Find each white blood cell.
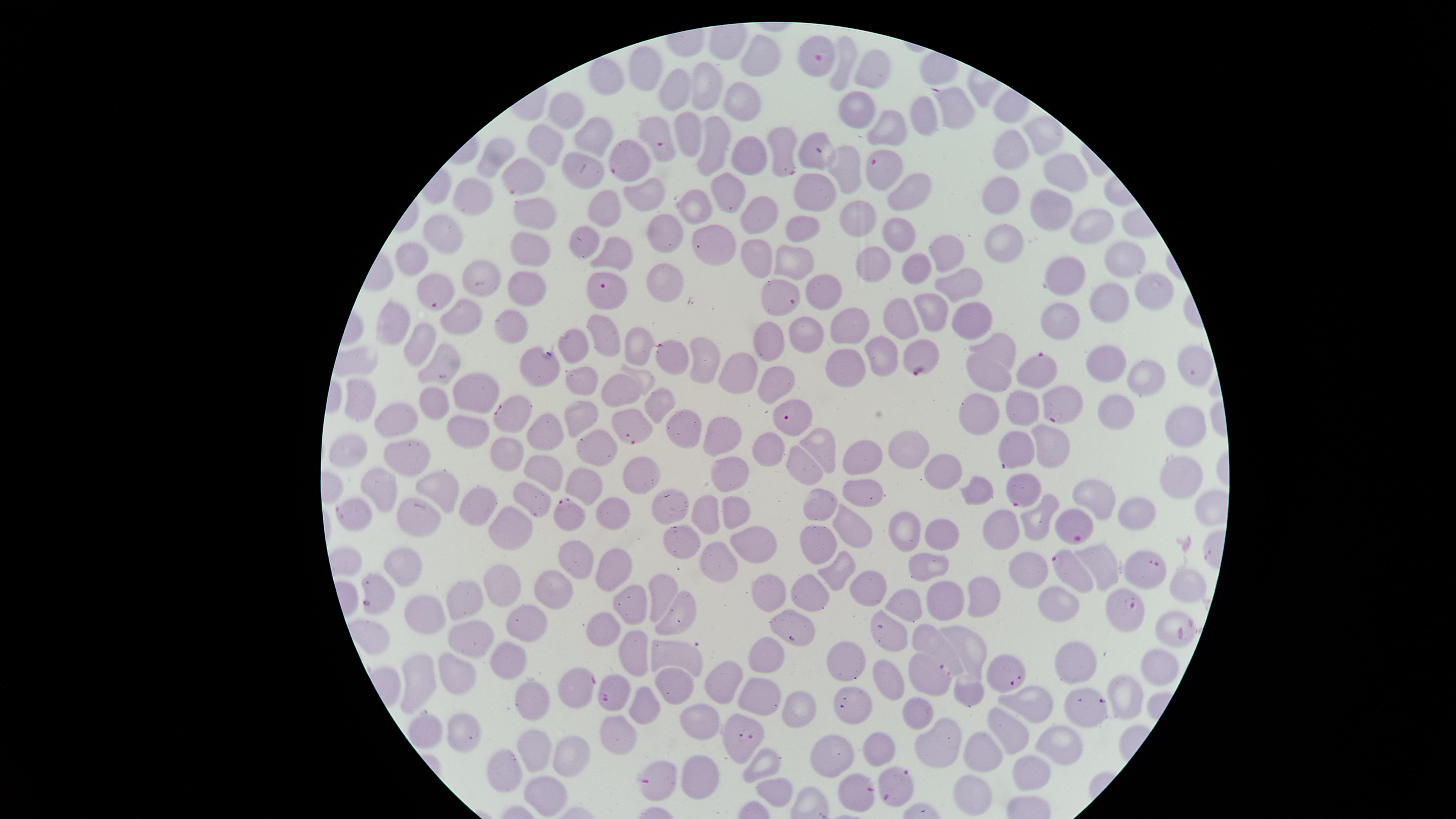

No white blood cells identified.

field of view = single
image size = 1456×819 pixels
parasitized red blood cells = approximate marker points as (x, y) in pixels: (819, 57), (949, 103), (658, 134), (780, 146), (815, 152), (627, 161), (884, 164), (521, 175), (609, 289), (439, 293), (781, 296), (671, 357), (919, 358), (1038, 370), (1062, 402), (514, 415), (793, 416), (629, 424), (1013, 448), (1021, 492), (361, 512), (568, 514), (1074, 525), (1070, 571), (1152, 573), (1126, 605), (1001, 670), (925, 672), (581, 685), (610, 695), (743, 738), (658, 777), (896, 786), (856, 795)
preparation = thin blood smear
species = Plasmodium falciparum
presence = malaria parasites seen
uninfected red blood cells = approximate marker points as (x, y) in pixels: (759, 57), (846, 68), (649, 72), (873, 72), (606, 75), (712, 86), (680, 88), (748, 99), (569, 109), (857, 111), (921, 115), (890, 129), (1045, 133), (686, 134), (596, 137), (714, 142), (548, 146), (1011, 150), (499, 154), (745, 154), (582, 161), (850, 166), (1070, 171), (911, 185), (642, 186), (815, 188), (729, 194), (1003, 194), (475, 195), (605, 202), (1050, 206), (696, 209), (859, 213), (536, 214), (756, 215), (1097, 218), (799, 228), (586, 234), (664, 234), (900, 236), (1012, 239), (440, 245), (947, 245), (713, 248), (527, 252), (616, 252), (418, 254), (1128, 258), (870, 260), (753, 263), (793, 267), (921, 267), (1067, 270), (485, 278), (964, 279), (668, 281), (526, 287), (819, 289), (1151, 293), (1111, 300), (931, 309), (903, 311), (459, 313), (396, 320), (1058, 320), (511, 322), (972, 323), (850, 326), (807, 332), (607, 334), (422, 339), (764, 340), (577, 342), (882, 348), (637, 349), (1007, 351), (1104, 356), (703, 361), (440, 363), (1197, 363), (844, 368), (739, 370), (539, 372), (985, 376), (583, 377), (645, 378), (775, 380), (1145, 380), (613, 387), (473, 389), (362, 396), (438, 404), (660, 404), (1028, 406), (972, 410), (1118, 410), (396, 417), (579, 418), (541, 427), (1186, 428), (470, 429), (685, 430), (719, 435), (1058, 445), (816, 447), (595, 448), (763, 449), (503, 451), (914, 451), (343, 455), (405, 456), (862, 457), (806, 463), (545, 471), (637, 473), (943, 473), (729, 475), (1179, 475), (379, 485), (583, 485), (978, 487), (441, 489), (861, 493), (1094, 493), (816, 500), (530, 503), (484, 505), (670, 509), (733, 510), (1138, 510), (616, 511), (705, 513), (420, 517), (854, 525), (1005, 525), (1036, 526), (509, 527), (906, 532), (941, 535), (679, 541), (748, 544), (813, 549), (578, 561), (712, 562), (614, 563), (394, 564), (927, 565), (1105, 567), (833, 569), (1033, 576), (501, 584), (1178, 586), (866, 587), (765, 592), (552, 593), (984, 595), (662, 596), (809, 598), (1062, 601), (951, 602), (466, 604), (908, 604), (636, 606), (431, 613), (679, 616), (529, 617), (799, 625), (1171, 626), (610, 627), (469, 633), (894, 635), (931, 641), (964, 648), (635, 649), (679, 650), (514, 655), (1158, 658), (769, 662), (1071, 662), (852, 665), (451, 674), (882, 679), (421, 682), (723, 682), (675, 683), (1120, 693), (968, 695), (532, 696), (757, 699), (1081, 699), (1034, 701), (849, 702), (647, 704), (795, 709), (917, 711), (694, 715), (1010, 729), (458, 731), (426, 732), (619, 732), (946, 742), (1067, 744), (533, 746), (877, 749), (983, 750), (567, 754), (835, 755), (765, 763), (504, 764), (1028, 769), (698, 773), (772, 786), (973, 795), (539, 798)
stain = Giemsa
visible region = circular
capture = smartphone photograph through the microscope eyepiece